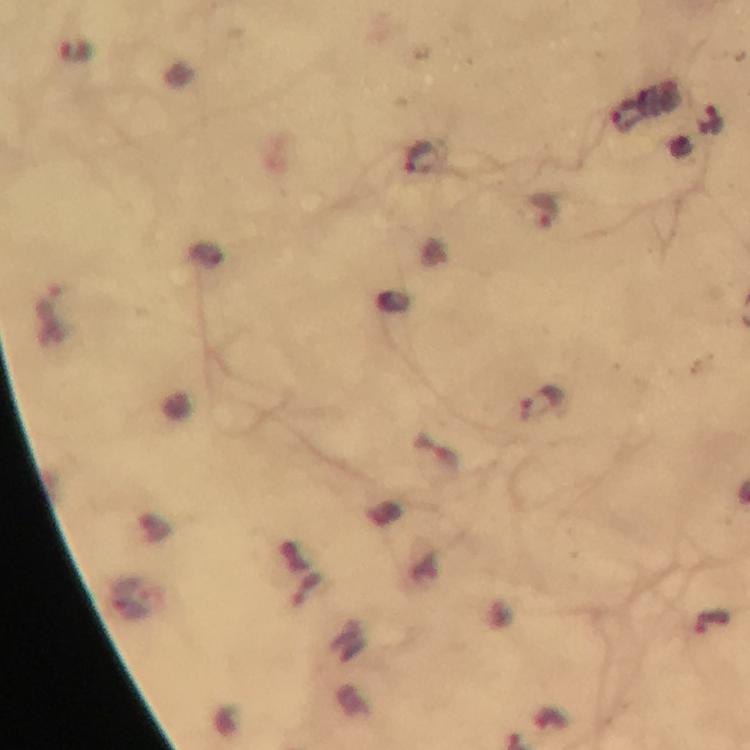
capture = smartphone mounted on the microscope
context = from a diagnostic examination for malaria
magnification = 100x
stain = Giemsa
cropped from = a single field of view
immersion oil = applied
malaria parasite locations = approximate centers as [x, y] in pixels: [77, 52], [709, 121], [542, 211], [542, 403], [714, 622]
preparation = thick blood smear
image size = 750×750 pixels